Assess this cell for malaria.
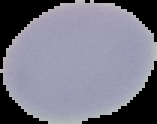

Uninfected.

From a thin blood smear. Image is 157×124 pixels. Segmented cell region on a black background.